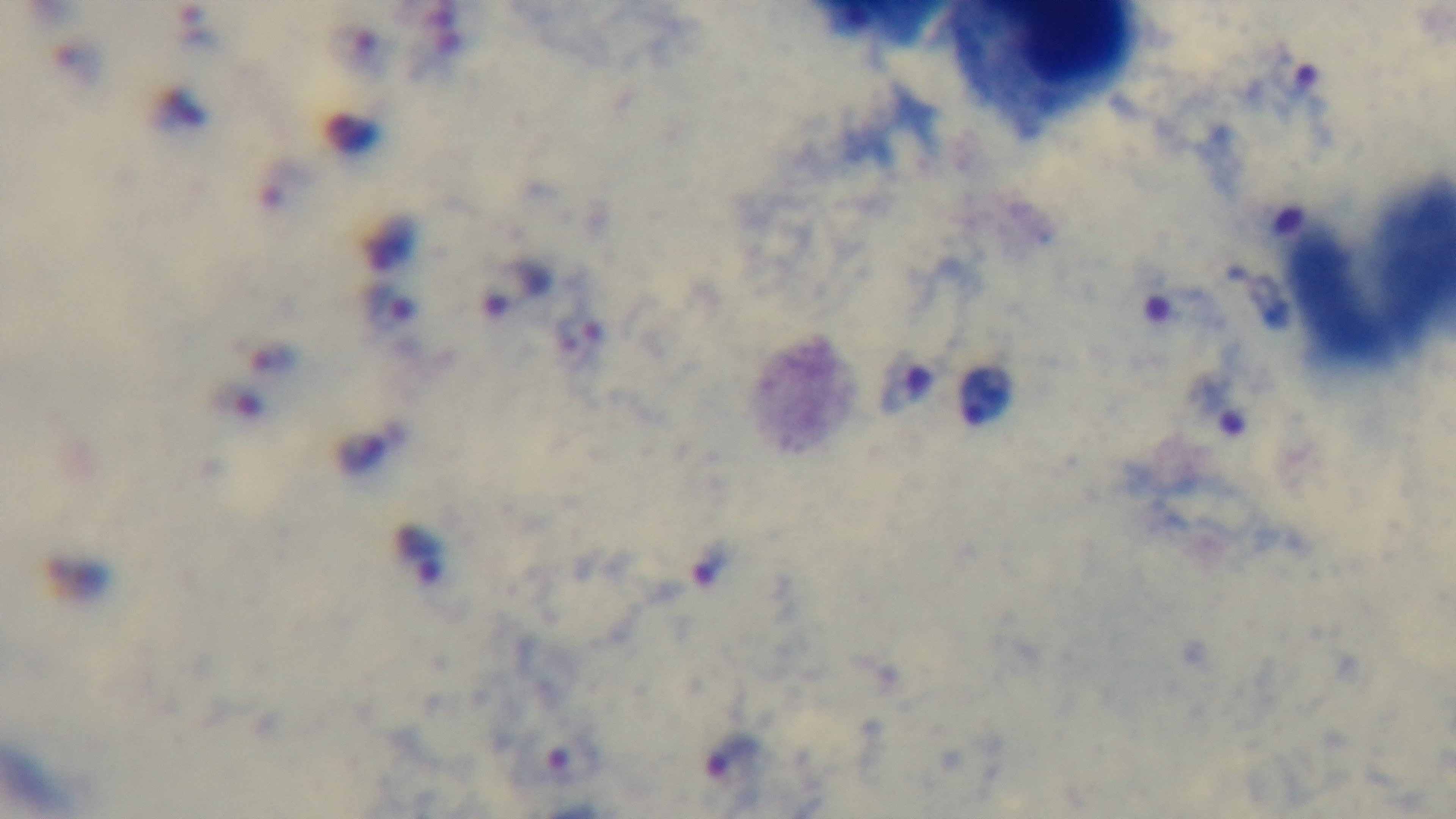
Summary:
  - Objective: 100x oil immersion
  - Stain: Giemsa
  - Preparation: thick smear
  - Modality: light microscopy
  - Field of view: single
  - Malaria status: positive
  - Capture: mounted 4K digital camera